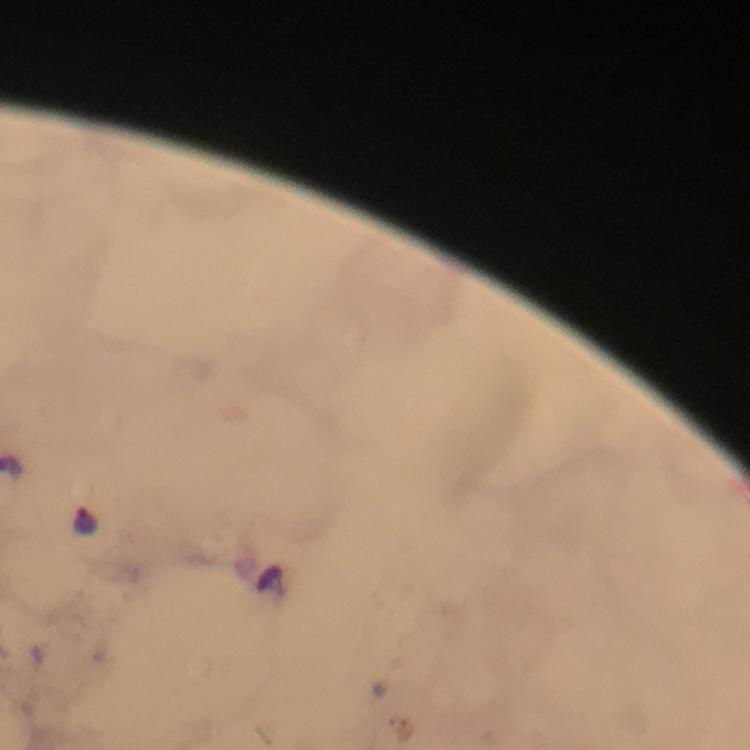
Approximate centers as {x, y} in pixels. Plasmodium parasite locations: {86, 518}. 100x magnification. Thick blood smear. Giemsa-stained preparation. Image is 750×750 pixels. Immersion oil applied. Cropped region of a single field of view. Smartphone photograph taken through a microscope. From a malaria diagnostic workup.